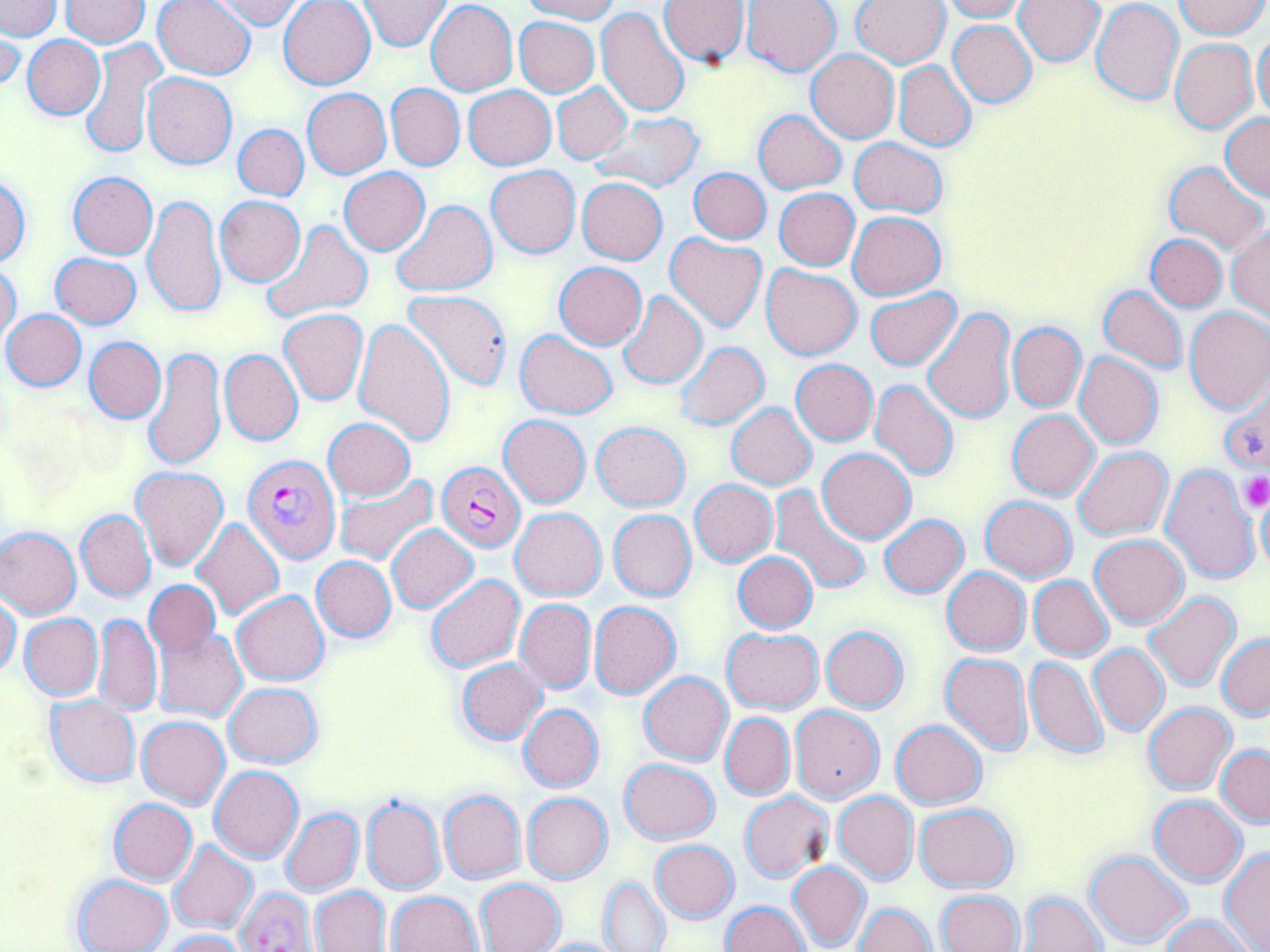
Plasmodium falciparum-infected red blood cell locations = approximate bounding boxes as (x1, y1, x2, y2) in pixels: (245, 453, 341, 563), (436, 462, 526, 552), (235, 889, 315, 952)
slide-level diagnosis = Plasmodium falciparum
magnification = 1000x
stain = May-Grünwald-Giemsa
image size = 1270×952 pixels
field of view = one of a larger specimen
uninfected red blood cell locations = approximate bounding boxes as (x1, y1, x2, y2) in pixels: (3, 0, 43, 64), (153, 0, 256, 79), (209, 0, 307, 30), (278, 0, 375, 89), (358, 0, 450, 51), (519, 0, 618, 23), (941, 0, 1029, 22), (1089, 0, 1183, 105), (1175, 0, 1267, 39), (0, 1, 61, 39), (61, 1, 151, 48), (426, 1, 517, 96), (658, 1, 751, 66), (740, 1, 840, 75), (850, 1, 950, 68), (1015, 1, 1103, 65), (597, 6, 690, 115), (514, 17, 600, 98), (948, 20, 1036, 107), (0, 28, 23, 95), (1254, 32, 1270, 123), (23, 35, 105, 119), (80, 38, 167, 161), (1170, 38, 1259, 132), (805, 49, 900, 143), (893, 60, 976, 151), (143, 73, 237, 169), (552, 82, 630, 165), (386, 84, 464, 169), (463, 86, 555, 170), (302, 88, 391, 179), (754, 111, 845, 193), (590, 112, 705, 192), (1221, 114, 1270, 200), (233, 123, 308, 200), (849, 138, 947, 218), (1163, 162, 1268, 256), (486, 165, 579, 258), (689, 167, 771, 244), (340, 169, 429, 254), (67, 172, 158, 259), (0, 174, 31, 267), (577, 178, 667, 264), (774, 187, 859, 270), (140, 194, 225, 321), (215, 196, 305, 285), (391, 199, 497, 296), (847, 211, 946, 300), (261, 220, 372, 323), (1227, 228, 1269, 321), (664, 233, 767, 333), (1147, 235, 1226, 312), (51, 252, 142, 328), (1, 262, 21, 344), (554, 262, 646, 349), (761, 264, 862, 360), (1099, 286, 1188, 372), (403, 287, 513, 390), (616, 290, 706, 388), (865, 290, 960, 370), (1185, 307, 1270, 412), (2, 308, 85, 390), (279, 308, 368, 405), (922, 308, 1016, 425), (354, 317, 455, 445), (1008, 323, 1085, 411), (515, 329, 617, 419), (84, 336, 165, 423), (676, 341, 769, 431), (143, 346, 226, 471), (219, 349, 302, 445), (1074, 353, 1162, 449), (792, 359, 878, 444), (1221, 378, 1270, 475), (869, 379, 959, 483), (726, 403, 817, 489), (1007, 409, 1099, 500), (500, 415, 590, 508), (323, 419, 415, 500), (593, 422, 688, 510), (1073, 447, 1172, 539), (817, 449, 915, 543), (1161, 463, 1263, 584), (132, 466, 228, 570), (335, 474, 438, 566), (690, 480, 777, 566), (768, 485, 872, 596), (980, 496, 1077, 582), (1257, 496, 1270, 572), (511, 507, 606, 601), (608, 509, 696, 601), (76, 510, 156, 602), (880, 514, 968, 597), (191, 519, 283, 620), (387, 525, 478, 612), (0, 527, 81, 618), (1090, 534, 1189, 629), (733, 552, 817, 633), (311, 556, 396, 641), (942, 567, 1031, 656), (426, 573, 525, 672), (1028, 576, 1114, 660), (145, 579, 221, 659), (232, 591, 329, 686), (1145, 592, 1242, 691), (0, 596, 21, 676), (515, 599, 596, 693), (590, 601, 680, 699), (94, 613, 162, 716), (20, 614, 103, 700), (154, 624, 246, 721), (819, 625, 909, 713), (721, 626, 824, 713), (1217, 634, 1270, 720), (1089, 643, 1170, 737), (941, 652, 1034, 755), (1024, 654, 1110, 759), (457, 659, 547, 745), (640, 671, 732, 765), (224, 683, 322, 768), (44, 695, 140, 789), (1144, 702, 1237, 794), (518, 703, 602, 792), (789, 705, 884, 804), (720, 713, 794, 800), (137, 716, 230, 808), (890, 719, 987, 808), (1216, 745, 1270, 826), (619, 758, 720, 845), (210, 766, 303, 862), (439, 790, 525, 883), (739, 791, 833, 882), (832, 791, 918, 885), (523, 792, 612, 883), (361, 794, 445, 896), (1149, 794, 1247, 886), (110, 798, 197, 885), (915, 802, 1017, 893), (280, 808, 363, 897), (650, 840, 739, 924), (167, 841, 257, 934), (1083, 850, 1192, 949), (1220, 850, 1270, 950), (789, 862, 871, 950), (71, 874, 173, 952), (598, 876, 671, 952), (476, 878, 565, 951), (312, 887, 389, 952), (935, 890, 1025, 952), (388, 891, 483, 952), (1022, 891, 1107, 952), (721, 901, 810, 952), (854, 902, 935, 952), (1164, 915, 1253, 952), (160, 930, 245, 952), (533, 937, 634, 952)
modality = light microscopy
platelet locations = approximate bounding boxes as (x1, y1, x2, y2) in pixels: (1240, 470, 1270, 511)
preparation = thin blood smear